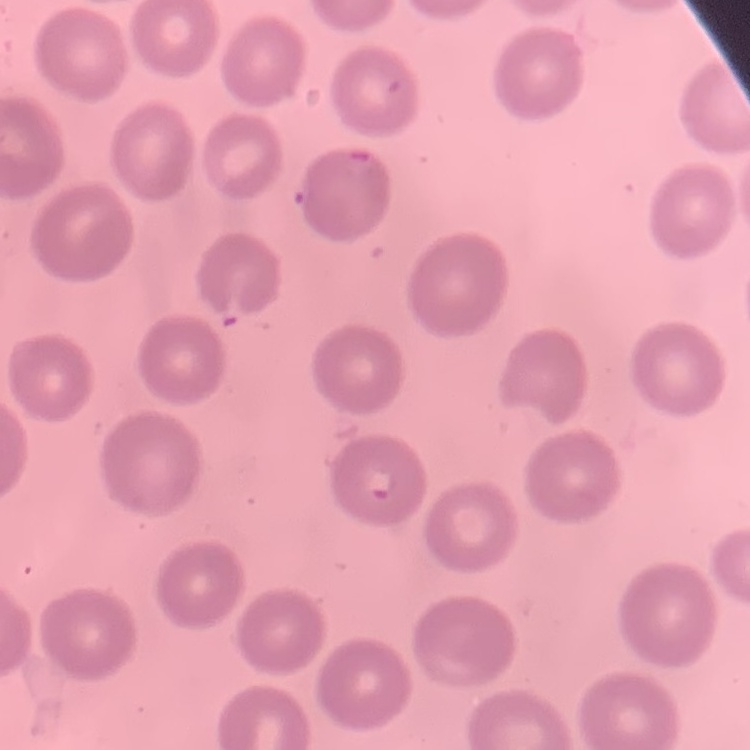 The red blood cells exhibit no rouleaux formation. Thin peripheral smear. One tile cut from a larger photomicrograph. Field's or Giemsa stain.